Identify the parasite.
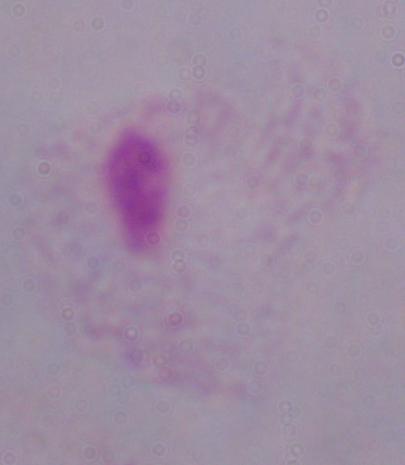
This is a trichomonad.

modality = photomicrograph
magnification = 1000x